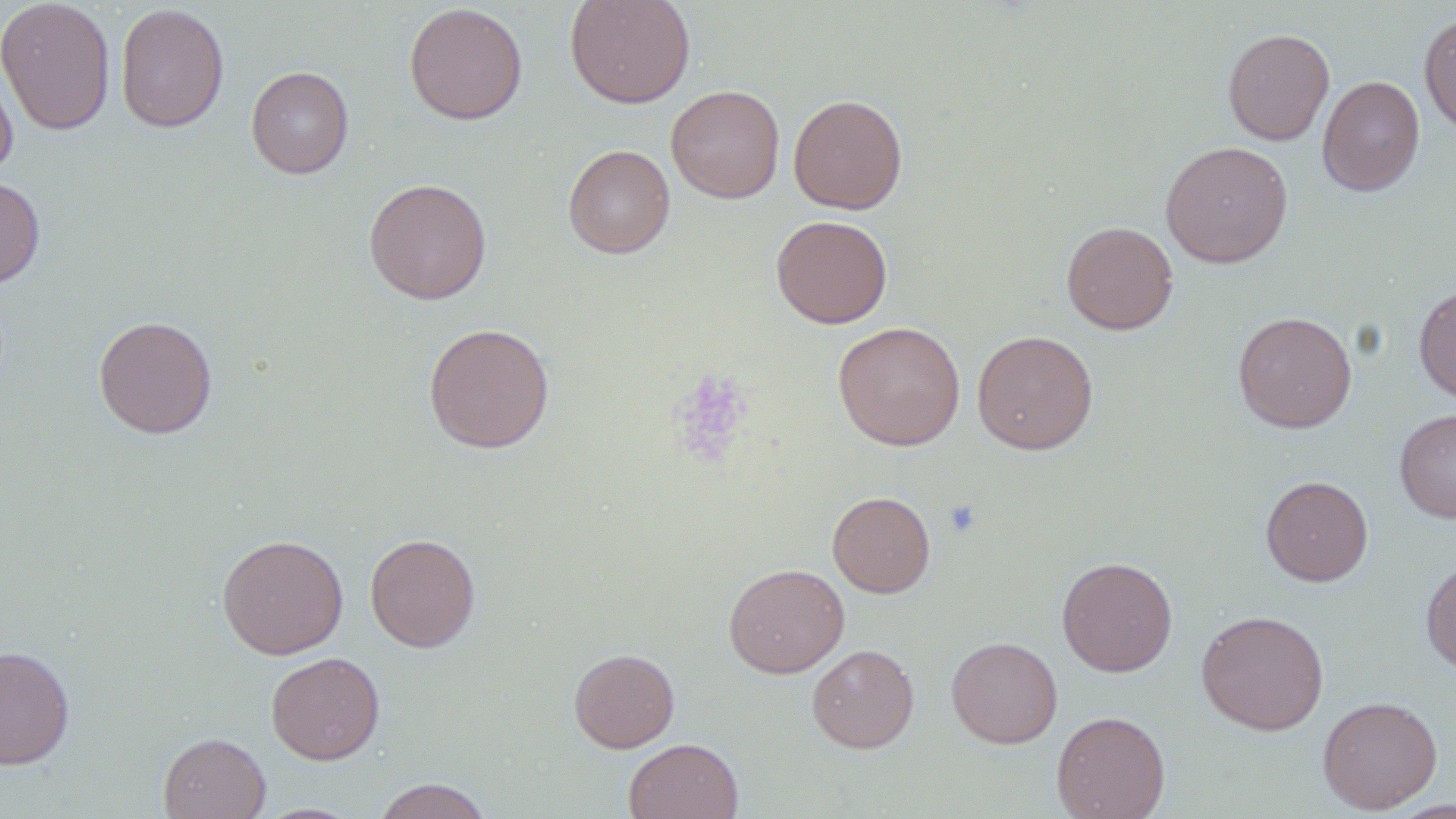

Approximate bounding boxes as (x1, y1, x2, y2) in pixels. Platelet locations: (672, 370, 754, 464), (943, 499, 981, 538). Uninfected red blood cell locations: (0, 0, 116, 135), (564, 0, 696, 109), (115, 2, 230, 133), (404, 2, 528, 125), (1418, 12, 1456, 137), (1222, 28, 1335, 146), (0, 57, 18, 180), (245, 65, 354, 179), (1317, 75, 1425, 196), (666, 84, 785, 202), (788, 94, 908, 214), (1160, 140, 1293, 268), (562, 144, 675, 258), (0, 175, 45, 290), (363, 178, 492, 304), (771, 214, 893, 329), (1061, 221, 1178, 335), (1414, 284, 1456, 405), (1232, 311, 1357, 433), (93, 315, 218, 438), (833, 321, 965, 451), (422, 322, 555, 454), (972, 330, 1098, 455), (1394, 407, 1456, 523), (1261, 475, 1373, 586), (827, 491, 936, 597), (365, 533, 481, 652), (217, 534, 348, 659), (1057, 556, 1178, 677), (1421, 559, 1456, 673), (723, 563, 849, 678), (1196, 609, 1329, 735), (946, 635, 1063, 748), (807, 644, 919, 753), (0, 646, 75, 769), (569, 647, 679, 753), (266, 651, 385, 764), (1317, 695, 1443, 814), (1051, 710, 1171, 819), (158, 732, 271, 819), (624, 738, 743, 819), (371, 778, 494, 819). Slide-level diagnosis: no evidence of blood parasites. Optical microscopy. One field of a larger specimen. Thin blood smear. Captured at 1000x magnification. Image is 1456×819 pixels. May-Grünwald-Giemsa stain.